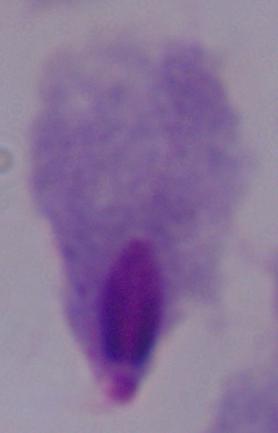
identification = trichomonad
modality = micrograph
magnification = 1000x